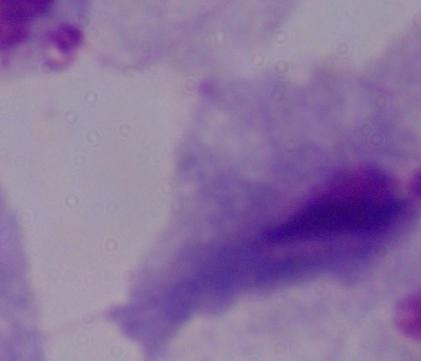
modality = photomicrograph
magnification = 1000x
identification = trichomonad